Classify this cell by malaria status.
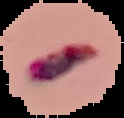
Parasitized.

Segmented cell region on a black background. From a thin blood smear. Image is 124×118 pixels.